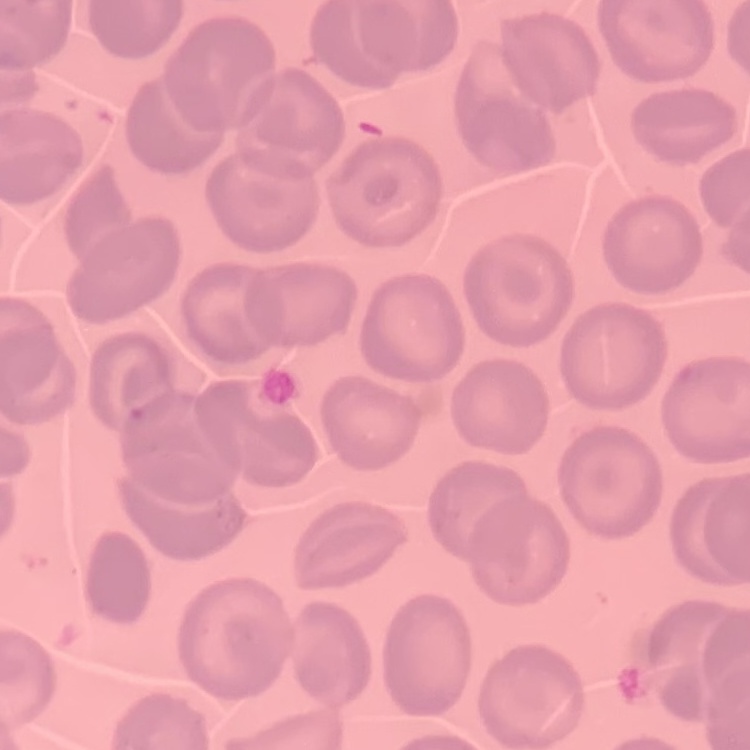
Summary:
  - Red blood cell morphology: no rouleaux formation
  - Image type: one tile cut from a larger photomicrograph
  - Stain: Field's or Giemsa
  - Preparation: thin blood film